State which parasite is depicted.
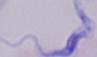

This is a trypanosome.

modality = photomicrograph
magnification = 1000x